Classify this cell by malaria status.
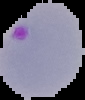
It is parasitized.

image type = cell region segmented out of the field of view; surrounding area masked to black
preparation = thin blood film
image size = 85×100 pixels